Name the cell type shown.
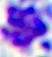
This is a leukocyte.

Micrograph. Captured at 400x magnification.